State the blood parasite species.
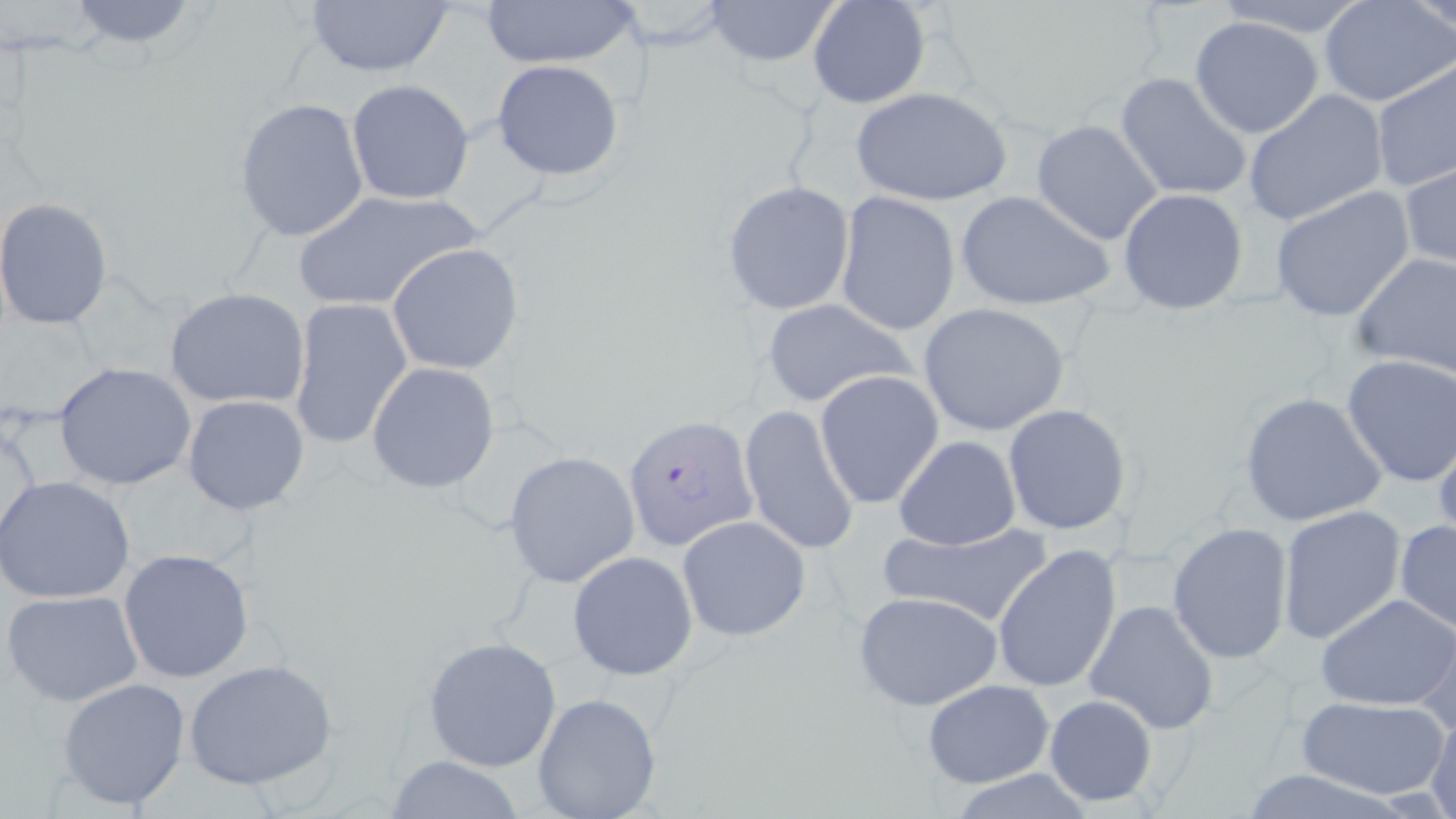

Plasmodium falciparum.

{
  "modality": "light microscopy",
  "plasmodium_falciparum_infected_red_blood_cell_locations": "approximate bounding boxes as named x1/y1/x2/y2 corners in pixels: (x1=623, y1=414, x2=758, y2=550)",
  "stain": "May-Grünwald-Giemsa",
  "field_of_view": "single",
  "uninfected_red_blood_cell_locations": "approximate bounding boxes as named x1/y1/x2/y2 corners in pixels: (x1=700, y1=0, x2=843, y2=72), (x1=807, y1=0, x2=931, y2=110), (x1=1209, y1=0, x2=1375, y2=36), (x1=1318, y1=0, x2=1456, y2=108), (x1=1409, y1=0, x2=1456, y2=34), (x1=60, y1=1, x2=207, y2=52), (x1=479, y1=1, x2=641, y2=70), (x1=604, y1=1, x2=737, y2=50), (x1=301, y1=2, x2=456, y2=79), (x1=1190, y1=16, x2=1325, y2=139), (x1=490, y1=58, x2=625, y2=181), (x1=1372, y1=62, x2=1456, y2=196), (x1=1114, y1=73, x2=1252, y2=203), (x1=345, y1=78, x2=475, y2=205), (x1=851, y1=88, x2=1012, y2=206), (x1=1243, y1=89, x2=1389, y2=227), (x1=234, y1=97, x2=369, y2=243), (x1=1032, y1=119, x2=1163, y2=245), (x1=1400, y1=161, x2=1456, y2=271), (x1=721, y1=181, x2=855, y2=317), (x1=1269, y1=187, x2=1416, y2=324), (x1=1118, y1=188, x2=1249, y2=315), (x1=292, y1=189, x2=483, y2=313), (x1=835, y1=190, x2=961, y2=337), (x1=955, y1=191, x2=1115, y2=311), (x1=0, y1=198, x2=114, y2=330), (x1=388, y1=242, x2=525, y2=375), (x1=1350, y1=251, x2=1456, y2=380), (x1=164, y1=286, x2=311, y2=411), (x1=288, y1=296, x2=414, y2=452), (x1=760, y1=298, x2=919, y2=409), (x1=918, y1=302, x2=1071, y2=435), (x1=1338, y1=354, x2=1456, y2=487), (x1=53, y1=361, x2=196, y2=491), (x1=366, y1=362, x2=499, y2=495), (x1=813, y1=368, x2=946, y2=509), (x1=1238, y1=390, x2=1386, y2=528), (x1=182, y1=395, x2=309, y2=516), (x1=738, y1=403, x2=860, y2=555), (x1=1002, y1=404, x2=1133, y2=536), (x1=1, y1=414, x2=46, y2=549), (x1=1432, y1=425, x2=1456, y2=546), (x1=893, y1=435, x2=1020, y2=551), (x1=503, y1=450, x2=642, y2=589), (x1=0, y1=476, x2=135, y2=605), (x1=1276, y1=506, x2=1407, y2=645), (x1=677, y1=515, x2=813, y2=642), (x1=1394, y1=520, x2=1456, y2=634), (x1=880, y1=522, x2=1055, y2=630), (x1=1167, y1=522, x2=1294, y2=667), (x1=992, y1=546, x2=1122, y2=694), (x1=117, y1=549, x2=257, y2=685), (x1=567, y1=551, x2=698, y2=680), (x1=3, y1=589, x2=143, y2=708), (x1=853, y1=590, x2=1005, y2=712), (x1=1315, y1=592, x2=1456, y2=712), (x1=1083, y1=600, x2=1220, y2=733), (x1=1411, y1=606, x2=1455, y2=740), (x1=422, y1=635, x2=563, y2=772), (x1=184, y1=657, x2=340, y2=791), (x1=56, y1=676, x2=192, y2=810), (x1=921, y1=678, x2=1054, y2=788), (x1=532, y1=692, x2=662, y2=819), (x1=1042, y1=692, x2=1160, y2=808), (x1=1298, y1=695, x2=1447, y2=799), (x1=1425, y1=709, x2=1456, y2=819), (x1=382, y1=754, x2=529, y2=819)",
  "magnification": "1000x",
  "image_size": "1456×819 pixels",
  "preparation": "thin blood film"
}